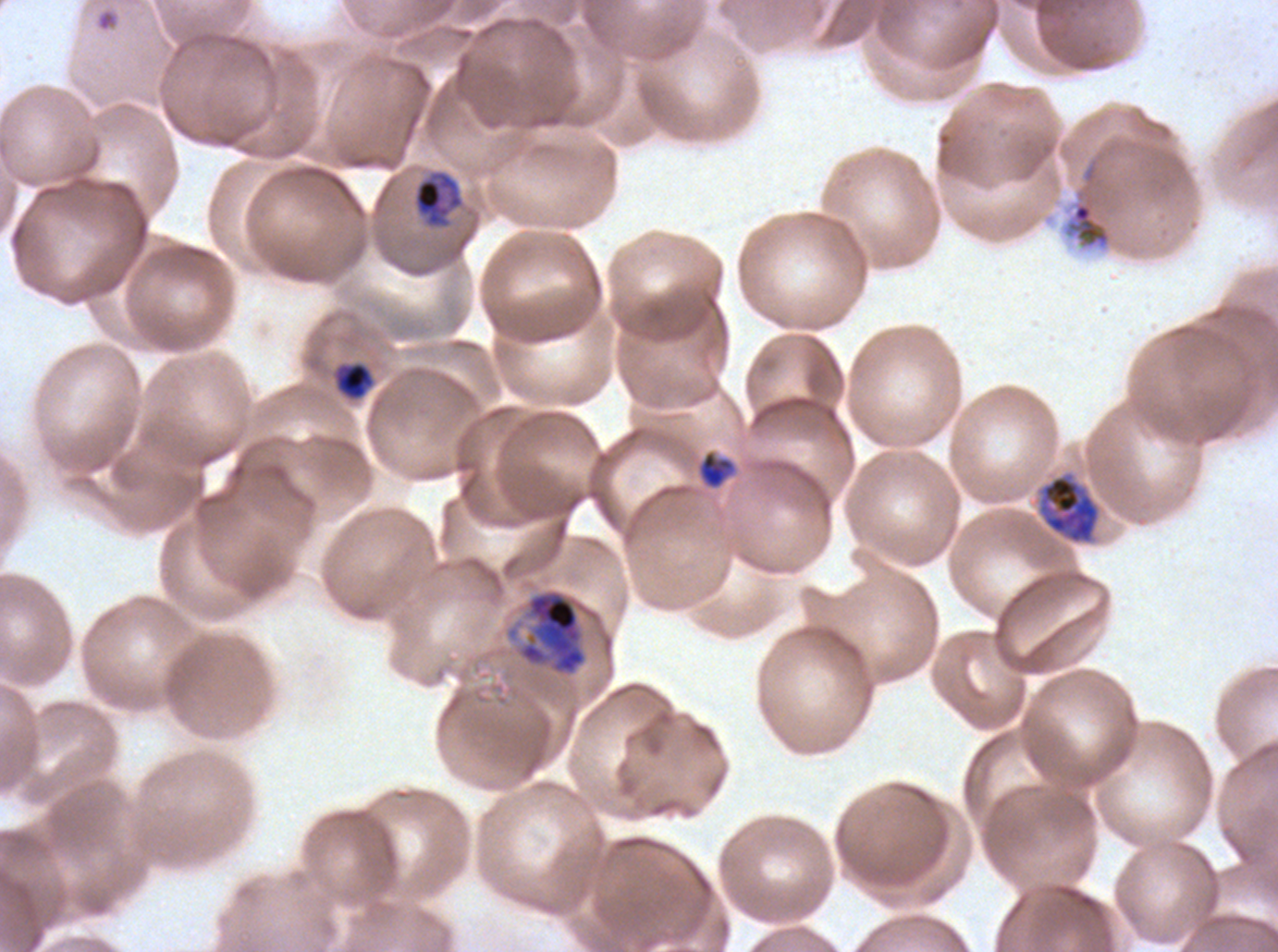

Approximate bounding rectangles given as corner coordinates in pixels from the top-left. Mid trophozoite locations: (x1=413, y1=170, x2=463, y2=227). Late trophozoite locations: (x1=1038, y1=473, x2=1100, y2=544). Ring locations: (x1=96, y1=9, x2=117, y2=31). Early schizont locations: (x1=518, y1=589, x2=587, y2=676). Late-ring/early-trophozoite locations: (x1=335, y1=361, x2=375, y2=400), (x1=697, y1=450, x2=735, y2=489). Debris locations: (x1=1065, y1=200, x2=1112, y2=249). One sub-image of a larger composite. Giemsa-stained preparation. Plasmodium falciparum from a patient in The Gambia, cultured ex vivo for 24 to 48 hours. Life-cycle stages observed: ring, late-ring/early-trophozoite, mid trophozoite, late trophozoite, early schizont. Thin blood film. Image is 1278×952 pixels.